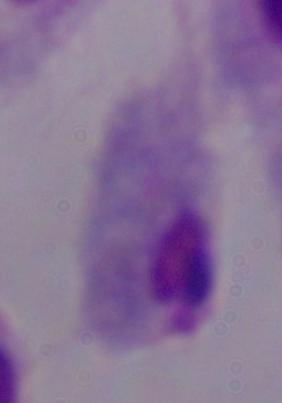

Photomicrograph. Captured at 1000x magnification. A trichomonad is shown.